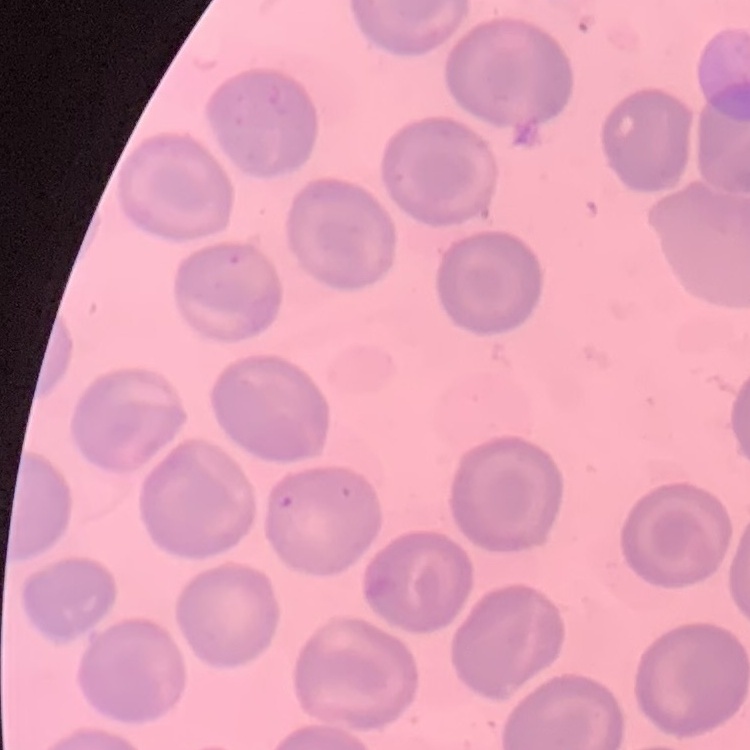
Summary:
  - Red blood cell morphology: no rouleaux formation
  - Image type: one tile cut from a larger photomicrograph
  - Preparation: thin peripheral smear
  - Stain: Field's or Giemsa